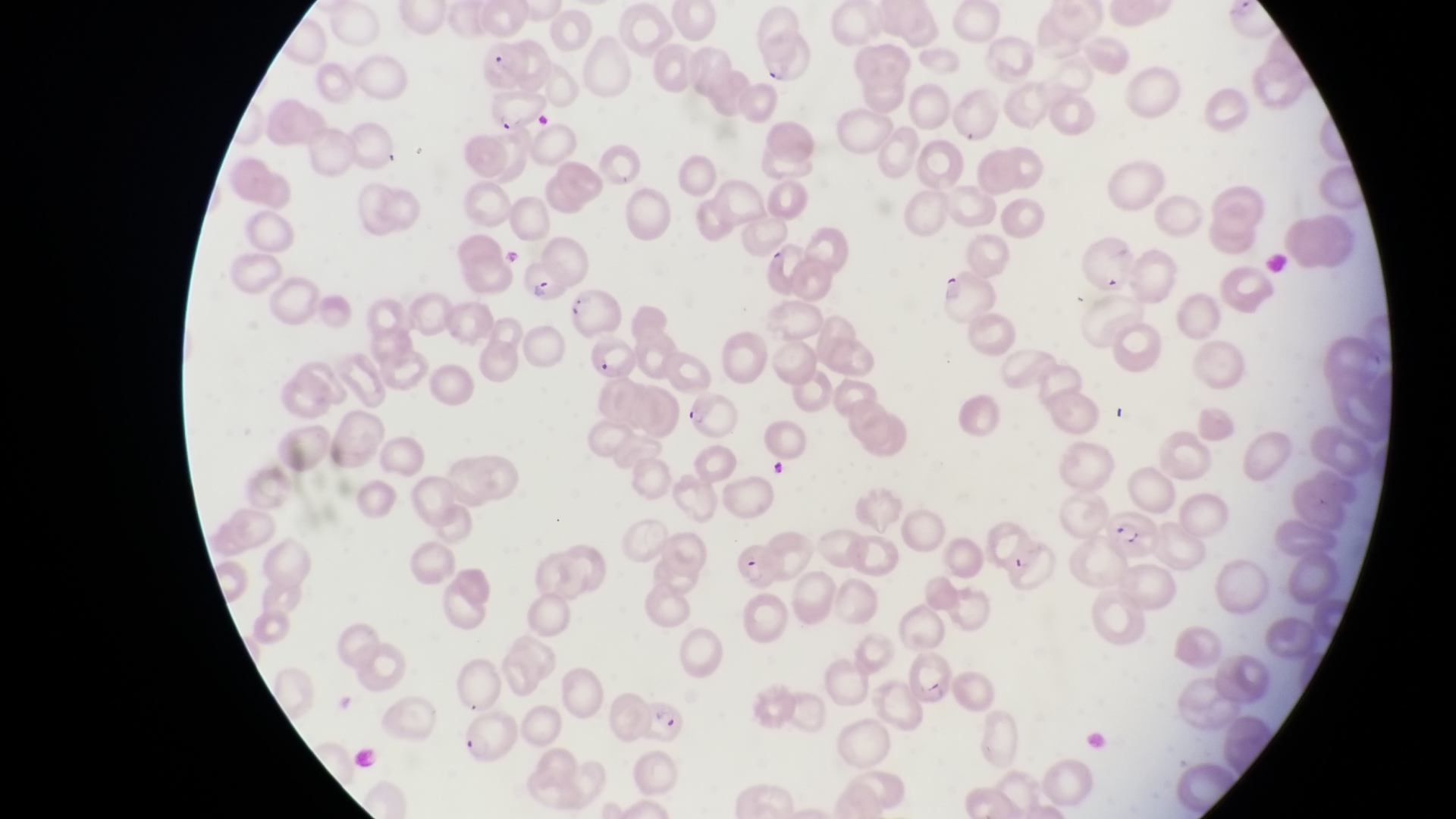
image_size: 1456×819 pixels
parasitised_red_blood_cell_locations: 'approximate bounding boxes as [left, top, right, bottom] in pixels: [752, 32, 815, 88], [475, 36, 533, 86], [485, 89, 549, 132], [523, 256, 573, 308], [588, 336, 640, 381], [686, 394, 742, 440], [1107, 510, 1156, 556], [736, 542, 783, 592], [644, 693, 699, 746]'
magnification: 1000x
field_of_view: single
capture: smartphone photograph through the eyepiece of an Olympus CX-23 microscope
country: Uganda
preparation: thin blood film